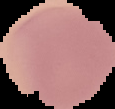

Summary:
  - Preparation: thin blood smear
  - Image size: 115×109 pixels
  - Malaria status: uninfected
  - Image type: segmented cell region on a black background